Classify this cell by malaria status.
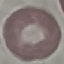

It is uninfected.

Photographed with a smartphone camera at the microscope eyepiece. Giemsa-stained preparation. Cell patch, automatically extracted from a larger field of view and resized to 64 × 64 pixels. Thin smear of blood.